Describe the morphology of the red blood cells.
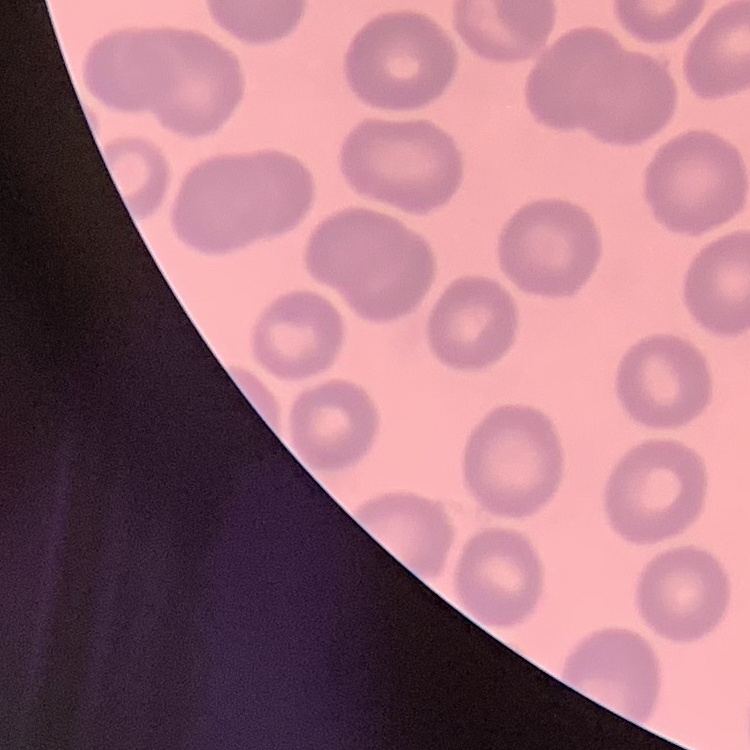
They show no rouleaux formation.

Thin blood film. One tile cut from a larger photomicrograph. Field's or Giemsa stain.